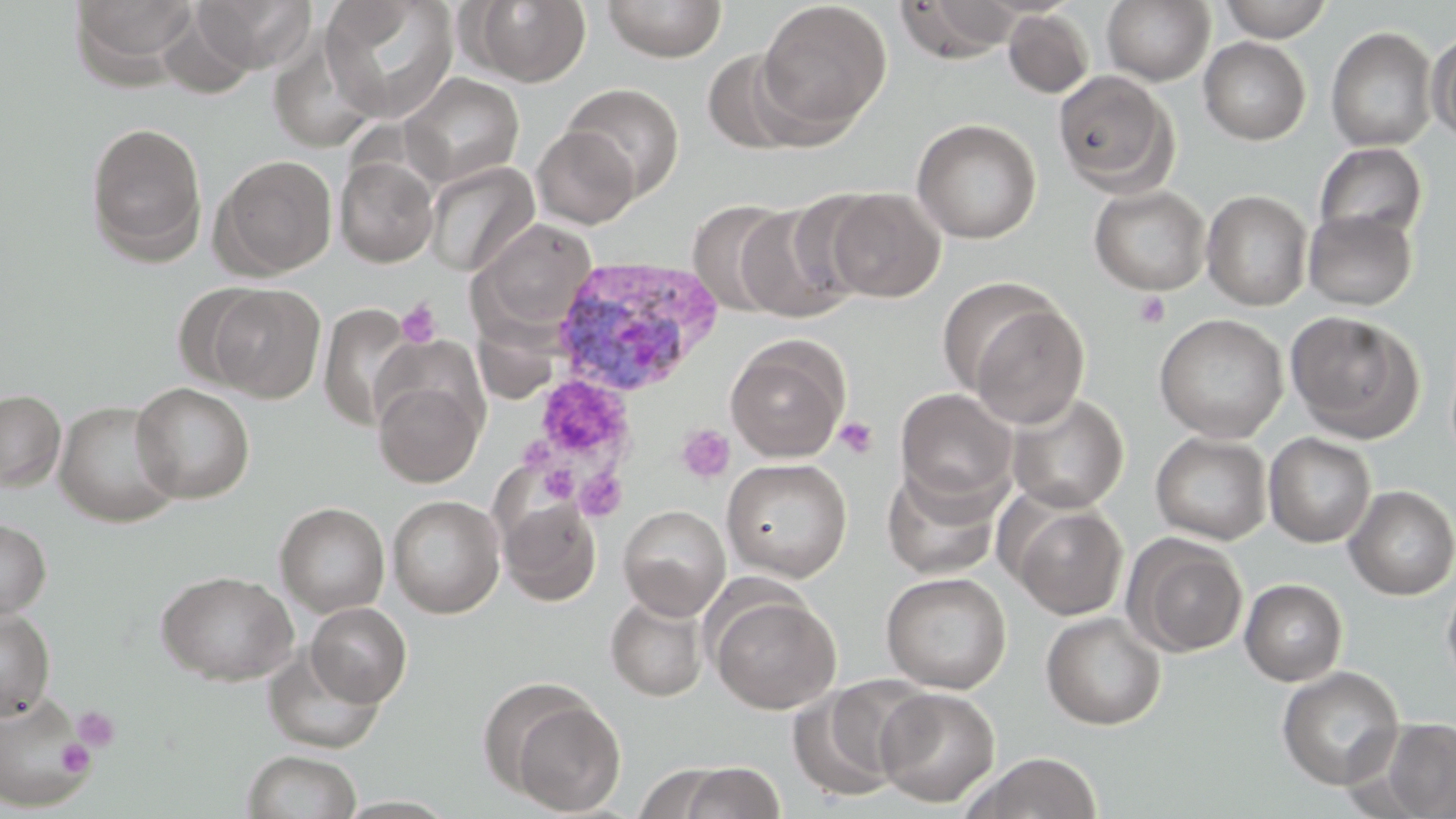 Approximate bounding boxes as (x1, y1, x2, y2) in pixels. Platelet locations: (1133, 291, 1171, 329), (396, 298, 441, 348), (536, 376, 629, 460), (834, 416, 878, 459), (676, 423, 735, 484), (539, 465, 579, 504), (575, 469, 627, 520), (72, 706, 121, 752), (55, 738, 95, 777). Uninfected red blood cell locations: (68, 0, 201, 85), (189, 0, 316, 76), (320, 0, 459, 122), (464, 0, 592, 87), (601, 0, 728, 62), (895, 0, 1024, 63), (1101, 0, 1216, 85), (1217, 0, 1332, 42), (757, 1, 892, 133), (1003, 8, 1095, 99), (1326, 26, 1437, 152), (1427, 27, 1456, 146), (266, 28, 380, 153), (1198, 37, 1311, 145), (701, 48, 817, 153), (1052, 70, 1179, 196), (399, 73, 524, 188), (562, 83, 684, 200), (911, 118, 1041, 244), (85, 122, 208, 265), (532, 127, 639, 228), (1314, 142, 1428, 242), (211, 154, 337, 279), (335, 154, 439, 267), (425, 161, 539, 277), (1088, 184, 1211, 295), (821, 187, 946, 302), (1201, 189, 1314, 310), (688, 199, 797, 317), (732, 201, 863, 323), (1303, 209, 1417, 310), (472, 219, 598, 333), (173, 283, 272, 391), (206, 283, 326, 403), (959, 293, 1090, 427), (318, 302, 417, 431), (1285, 311, 1425, 442), (1153, 314, 1288, 443), (472, 319, 559, 404), (725, 336, 849, 462), (372, 363, 487, 489), (131, 382, 255, 504), (895, 388, 1018, 508), (0, 389, 66, 492), (1005, 392, 1129, 513), (54, 400, 182, 528), (1151, 432, 1272, 545), (1264, 432, 1376, 548), (721, 458, 852, 582), (882, 469, 1001, 580), (1344, 485, 1456, 600), (387, 495, 505, 618), (498, 498, 602, 607), (1007, 500, 1129, 620), (275, 502, 390, 618), (618, 504, 730, 620), (0, 517, 51, 621), (1124, 535, 1248, 658), (156, 570, 299, 685), (881, 572, 1011, 693), (1442, 573, 1456, 691), (1240, 579, 1347, 685), (710, 592, 842, 714), (605, 593, 709, 702), (306, 602, 412, 707), (0, 607, 56, 721), (1041, 612, 1167, 730), (262, 647, 384, 754), (1276, 666, 1405, 790), (786, 678, 927, 803), (875, 687, 1000, 807), (0, 690, 95, 813), (501, 693, 627, 816), (1379, 718, 1456, 819), (241, 750, 362, 819), (969, 752, 1103, 818), (677, 762, 786, 818), (633, 763, 734, 819). Plasmodium vivax-infected red blood cell locations: (551, 256, 723, 398). Slide-level diagnosis: Plasmodium vivax. Captured at 1000x magnification. Image is 1456×819 pixels. One field of a larger specimen. May-Grünwald-Giemsa stain. Thin blood film. Light microscopy.